State the blood parasite species.
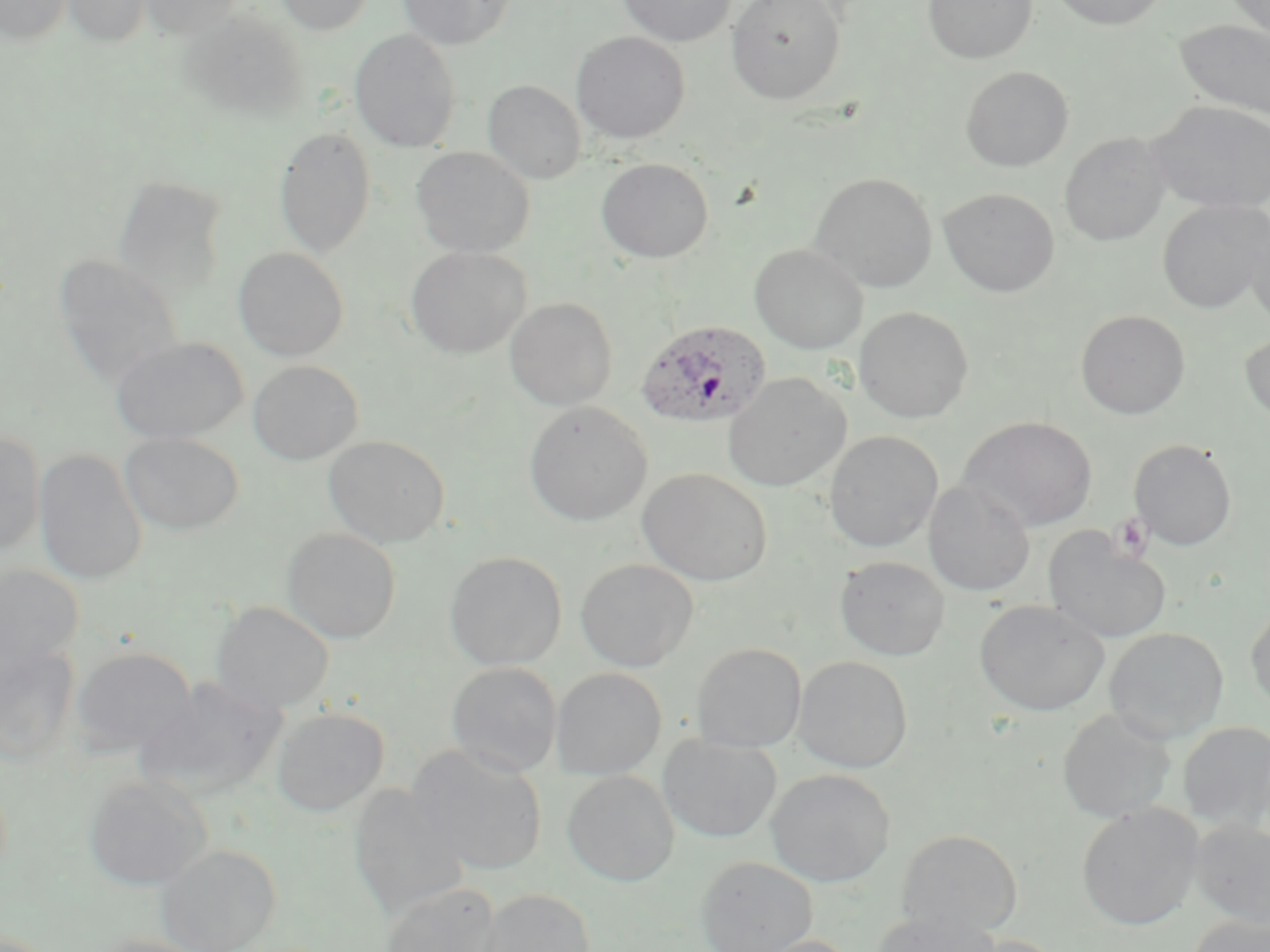

Plasmodium ovale.

Summary:
  - Coordinate format: approximate bounding boxes as named x1/y1/x2/y2 corners in pixels
  - Plasmodium ovale-infected red blood cell locations: (x1=636, y1=320, x2=771, y2=430)
  - Uninfected red blood cell locations: (x1=0, y1=0, x2=71, y2=45), (x1=62, y1=0, x2=150, y2=47), (x1=141, y1=0, x2=244, y2=38), (x1=276, y1=0, x2=375, y2=35), (x1=398, y1=0, x2=515, y2=49), (x1=617, y1=0, x2=736, y2=47), (x1=726, y1=0, x2=846, y2=104), (x1=923, y1=0, x2=1037, y2=64), (x1=1048, y1=0, x2=1172, y2=30), (x1=1224, y1=0, x2=1270, y2=42), (x1=179, y1=8, x2=308, y2=123), (x1=1174, y1=18, x2=1270, y2=121), (x1=350, y1=28, x2=461, y2=152), (x1=571, y1=31, x2=690, y2=144), (x1=960, y1=66, x2=1073, y2=171), (x1=483, y1=80, x2=586, y2=185), (x1=1148, y1=100, x2=1270, y2=213), (x1=274, y1=126, x2=377, y2=259), (x1=1059, y1=132, x2=1172, y2=246), (x1=411, y1=146, x2=535, y2=258), (x1=595, y1=157, x2=713, y2=263), (x1=810, y1=172, x2=938, y2=292), (x1=114, y1=175, x2=230, y2=299), (x1=938, y1=187, x2=1060, y2=297), (x1=1157, y1=200, x2=1270, y2=313), (x1=1245, y1=216, x2=1270, y2=329), (x1=749, y1=244, x2=868, y2=354), (x1=405, y1=246, x2=531, y2=358), (x1=232, y1=247, x2=349, y2=361), (x1=53, y1=254, x2=185, y2=391), (x1=504, y1=297, x2=618, y2=410), (x1=854, y1=306, x2=974, y2=423), (x1=1076, y1=309, x2=1191, y2=419), (x1=1239, y1=328, x2=1270, y2=427), (x1=110, y1=336, x2=249, y2=444), (x1=248, y1=360, x2=362, y2=465), (x1=723, y1=373, x2=851, y2=491), (x1=524, y1=402, x2=653, y2=526), (x1=958, y1=416, x2=1098, y2=532), (x1=0, y1=430, x2=45, y2=555), (x1=824, y1=430, x2=943, y2=552), (x1=120, y1=432, x2=244, y2=535), (x1=323, y1=435, x2=450, y2=547), (x1=1128, y1=438, x2=1237, y2=551), (x1=34, y1=448, x2=147, y2=586), (x1=637, y1=467, x2=773, y2=586), (x1=923, y1=480, x2=1035, y2=597), (x1=282, y1=527, x2=401, y2=643), (x1=1043, y1=528, x2=1172, y2=645), (x1=445, y1=550, x2=567, y2=670), (x1=834, y1=555, x2=950, y2=660), (x1=575, y1=558, x2=699, y2=671), (x1=0, y1=564, x2=84, y2=673), (x1=974, y1=599, x2=1109, y2=716), (x1=1245, y1=600, x2=1270, y2=715), (x1=211, y1=601, x2=334, y2=714), (x1=1104, y1=627, x2=1229, y2=743), (x1=0, y1=642, x2=81, y2=765), (x1=691, y1=642, x2=806, y2=751), (x1=70, y1=646, x2=196, y2=757), (x1=794, y1=655, x2=913, y2=772), (x1=446, y1=661, x2=562, y2=778), (x1=551, y1=667, x2=666, y2=779), (x1=136, y1=678, x2=287, y2=801), (x1=271, y1=707, x2=389, y2=816), (x1=1057, y1=709, x2=1177, y2=823), (x1=1178, y1=721, x2=1270, y2=833), (x1=658, y1=734, x2=782, y2=842), (x1=409, y1=744, x2=547, y2=875), (x1=766, y1=768, x2=896, y2=886), (x1=562, y1=770, x2=680, y2=886), (x1=83, y1=774, x2=211, y2=890), (x1=348, y1=783, x2=469, y2=921), (x1=1076, y1=803, x2=1203, y2=930), (x1=1190, y1=818, x2=1270, y2=929), (x1=897, y1=829, x2=1023, y2=936), (x1=155, y1=843, x2=280, y2=952), (x1=696, y1=856, x2=817, y2=952), (x1=380, y1=883, x2=500, y2=952), (x1=476, y1=888, x2=595, y2=952), (x1=869, y1=910, x2=1000, y2=952), (x1=1186, y1=915, x2=1270, y2=952), (x1=85, y1=934, x2=220, y2=952), (x1=741, y1=934, x2=860, y2=952), (x1=960, y1=934, x2=1068, y2=952)
  - Platelet locations: (x1=1111, y1=512, x2=1155, y2=562)
  - Magnification: 1000x
  - Modality: optical microscopy
  - Image size: 1270×952 pixels
  - Field of view: single
  - Stain: May-Grünwald-Giemsa
  - Preparation: thin blood film